Classify this cell by malaria status.
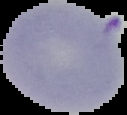
Parasitized.

Summary:
  - Image type: segmented cell region with the area outside set to black
  - Image size: 127×115 pixels
  - Preparation: thin blood film